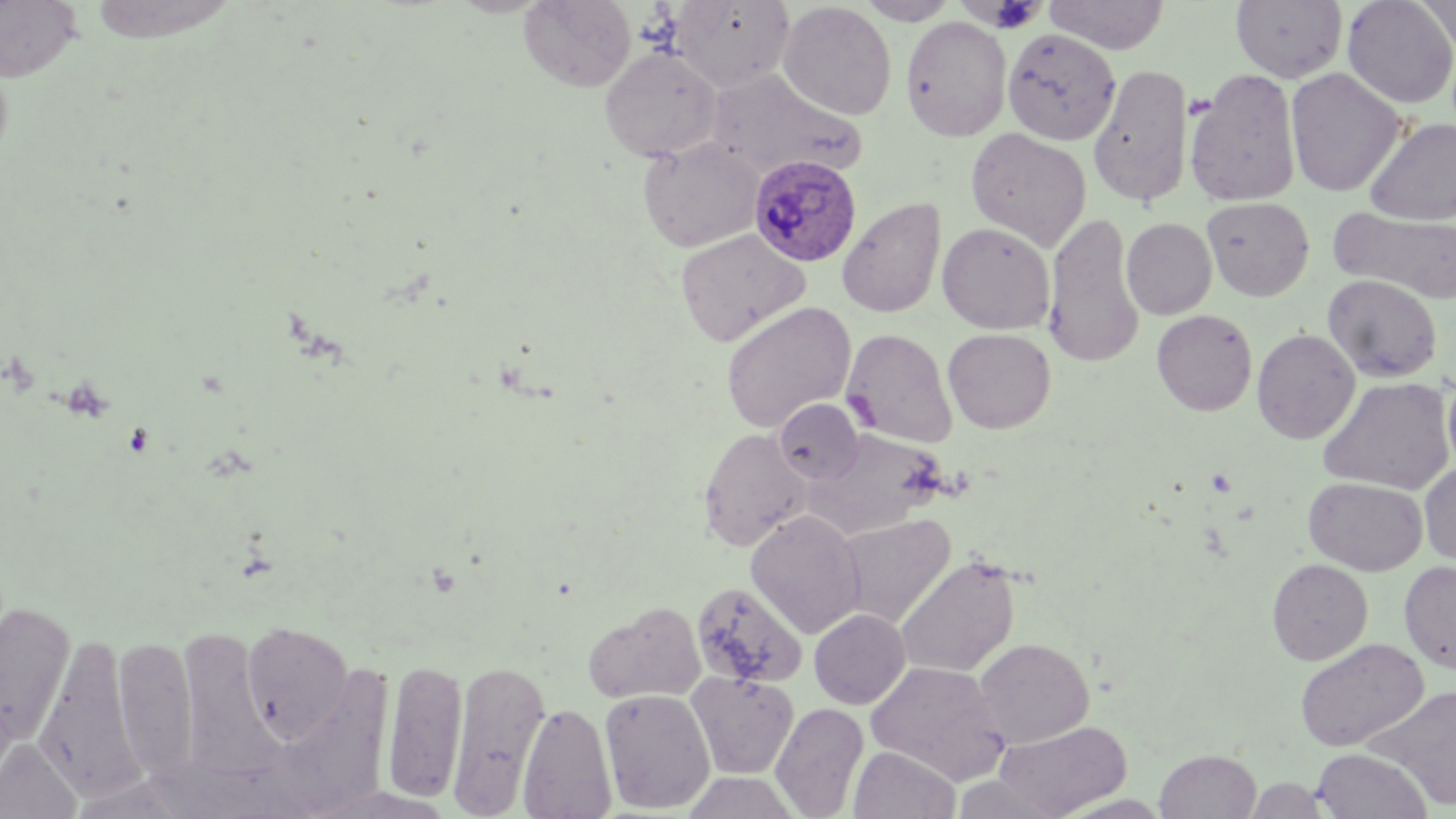

Approximate bounding boxes as (x1,y1)-(x2,y2) corner pairs in pixels. Plasmodium ovale-infected red blood cell locations: (748,153)-(862,267). Uninfected red blood cell locations: (0,0)-(82,82), (519,0)-(636,92), (856,0)-(960,25), (1043,0)-(1170,54), (1230,0)-(1348,83), (1342,0)-(1456,108), (1414,0)-(1456,55), (669,1)-(794,93), (778,1)-(897,120), (900,16)-(1012,141), (1003,29)-(1121,146), (599,45)-(723,162), (1088,63)-(1194,209), (1185,68)-(1302,208), (1285,68)-(1407,197), (705,70)-(862,181), (1364,117)-(1456,225), (966,128)-(1091,251), (638,137)-(764,252), (1202,196)-(1314,301), (837,197)-(945,318), (1330,205)-(1456,304), (1043,211)-(1145,368), (1121,217)-(1217,320), (937,222)-(1055,335), (675,228)-(809,346), (1322,274)-(1442,382), (720,302)-(856,434), (1152,309)-(1258,416), (841,328)-(957,447), (942,328)-(1056,433), (1252,328)-(1361,444), (1443,371)-(1456,475), (1317,376)-(1455,495), (774,399)-(864,485), (696,427)-(812,551), (804,429)-(948,539), (1419,461)-(1456,565), (1303,476)-(1427,576), (745,510)-(865,638), (836,512)-(956,628), (895,555)-(1019,678), (1267,558)-(1373,665), (1399,561)-(1456,672), (691,580)-(808,689), (0,601)-(75,744), (582,601)-(705,705), (809,608)-(911,709), (241,621)-(354,743), (178,627)-(277,780), (33,634)-(144,803), (113,636)-(197,782), (974,638)-(1094,748), (1294,638)-(1429,752), (382,658)-(467,803), (447,659)-(551,815), (865,660)-(1011,784), (687,671)-(798,779), (1369,685)-(1456,811), (599,688)-(716,813), (518,702)-(617,819), (771,702)-(869,818), (993,719)-(1133,818), (0,739)-(82,819), (849,745)-(960,818), (1312,747)-(1432,818), (1154,749)-(1261,819), (681,771)-(800,818), (1243,776)-(1332,818), (1051,793)-(1175,818). Slide-level diagnosis: Plasmodium ovale. Captured at 1000x magnification. May-Grünwald-Giemsa-stained preparation. Single field of view. Image is 1456×819 pixels. Light microscopy. Thin blood smear.